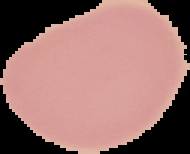

Summary:
  - Preparation: thin blood film
  - Image size: 190×154 pixels
  - Malaria status: uninfected
  - Image type: cell region segmented out of the field of view; surrounding area masked to black